Classify this cell by malaria status.
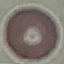

It is uninfected.

Cell patch, automatically extracted from a larger field of view and resized to 64 × 64 pixels. Giemsa stain. Thin blood film. Acquired by smartphone through the microscope eyepiece.